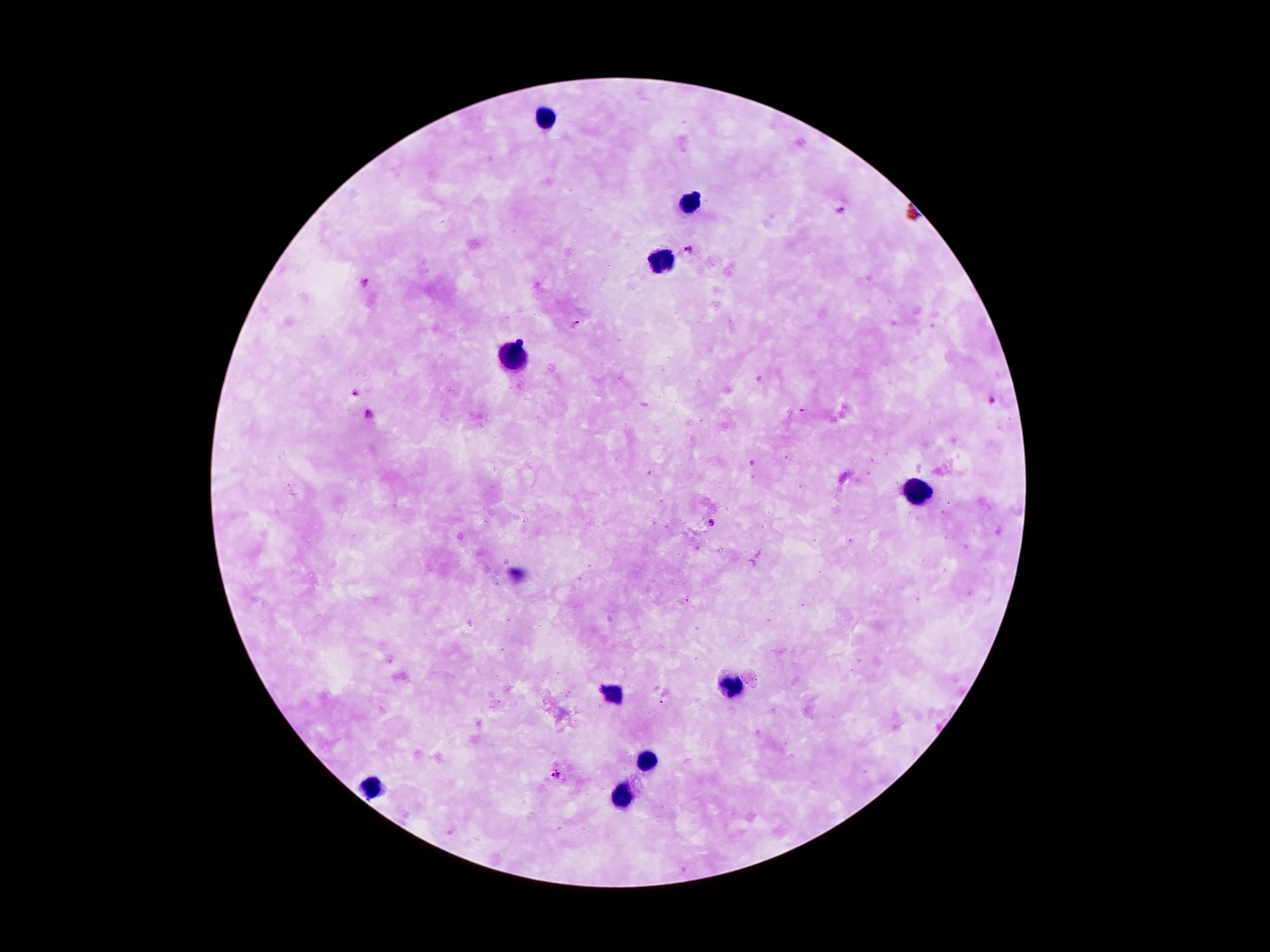

100x magnification. Photographed through the microscope eyepiece with a smartphone camera. Patient malaria status: positive for Plasmodium falciparum. Image is 1270×952 pixels. Giemsa-stained preparation. Thick blood smear. One field from this slide.